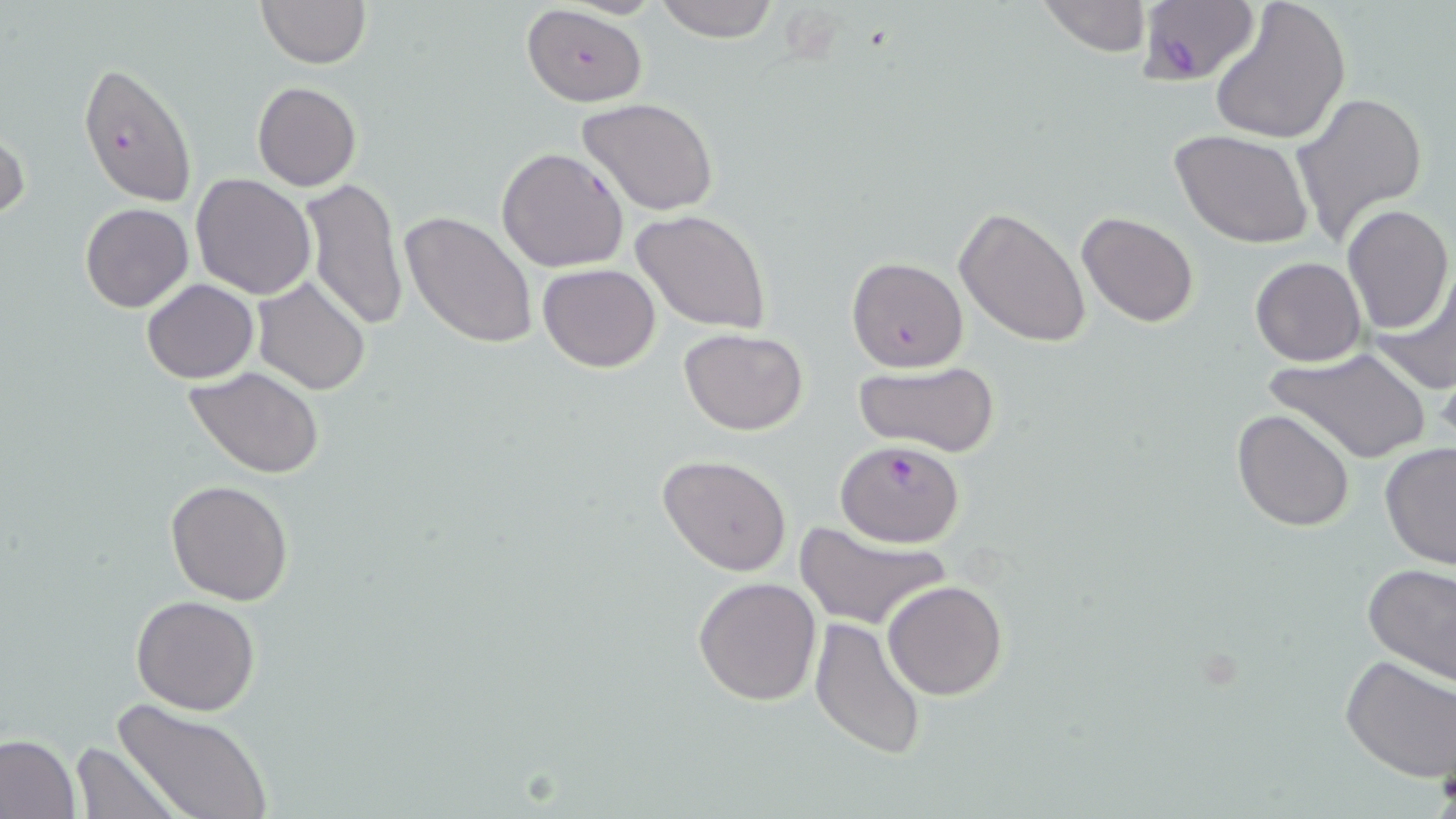

slide-level diagnosis = Plasmodium falciparum
image size = 1456×819 pixels
modality = optical microscopy
stain = May-Grünwald-Giemsa
Plasmodium falciparum-infected red blood cell locations = approximate bounding boxes as (x1, y1, x2, y2) in pixels: (1137, 1, 1260, 86), (520, 4, 648, 108), (78, 62, 198, 207), (497, 147, 629, 274), (840, 257, 964, 375), (835, 441, 964, 547)
uninfected red blood cell locations = approximate bounding boxes as (x1, y1, x2, y2) in pixels: (256, 0, 370, 68), (651, 0, 781, 43), (1036, 0, 1152, 56), (1208, 0, 1353, 145), (252, 82, 362, 192), (1291, 91, 1428, 244), (575, 97, 720, 219), (0, 124, 28, 226), (1169, 129, 1316, 249), (190, 173, 316, 299), (299, 178, 408, 332), (80, 202, 193, 313), (1340, 204, 1452, 334), (954, 206, 1092, 348), (630, 210, 771, 334), (1076, 210, 1200, 328), (400, 211, 538, 349), (1250, 257, 1367, 367), (1371, 259, 1456, 395), (538, 263, 661, 373), (252, 275, 371, 394), (141, 279, 259, 384), (680, 326, 807, 435), (1267, 345, 1434, 464), (854, 361, 1000, 455), (185, 367, 325, 479), (1232, 409, 1356, 531), (1378, 440, 1456, 569), (656, 453, 793, 576), (165, 480, 294, 604), (795, 522, 951, 632), (1362, 563, 1456, 687), (693, 575, 823, 706), (882, 580, 1008, 700), (132, 596, 259, 715), (809, 617, 927, 761), (1339, 654, 1455, 782), (114, 700, 271, 819), (0, 732, 81, 819), (72, 742, 182, 819)
magnification = 1000x
preparation = thin blood smear
field of view = single